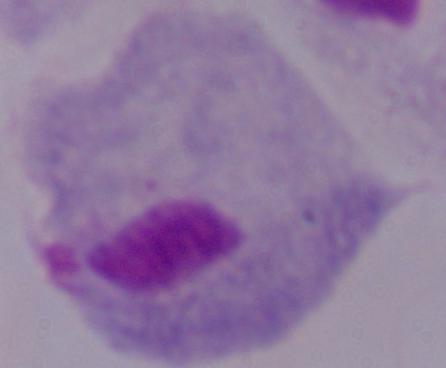
identification = trichomonad
modality = photomicrograph
magnification = 1000x